Locate Plasmodium parasites and leukocytes.
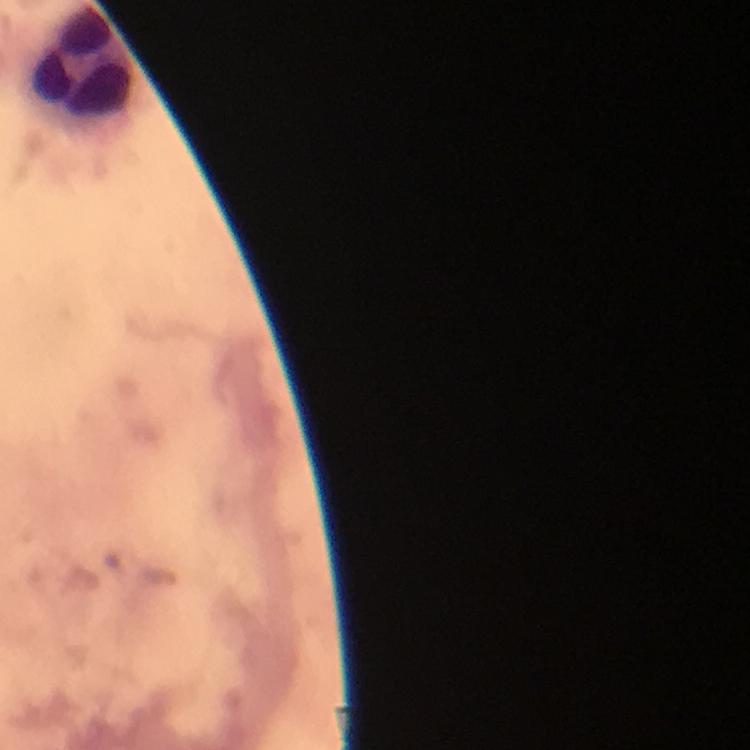

No Plasmodium parasites detected.
Approximate centers as (x, y) in pixels.
Leukocytes: (79, 60).

Summary:
  - Stain: Giemsa
  - Cropped from: a single field of view
  - Capture: smartphone mounted on the microscope
  - Preparation: thick blood film
  - Context: from a malaria diagnostic workup
  - Magnification: 100x
  - Image size: 750×750 pixels
  - Immersion oil: used